Locate every Plasmodium parasite.
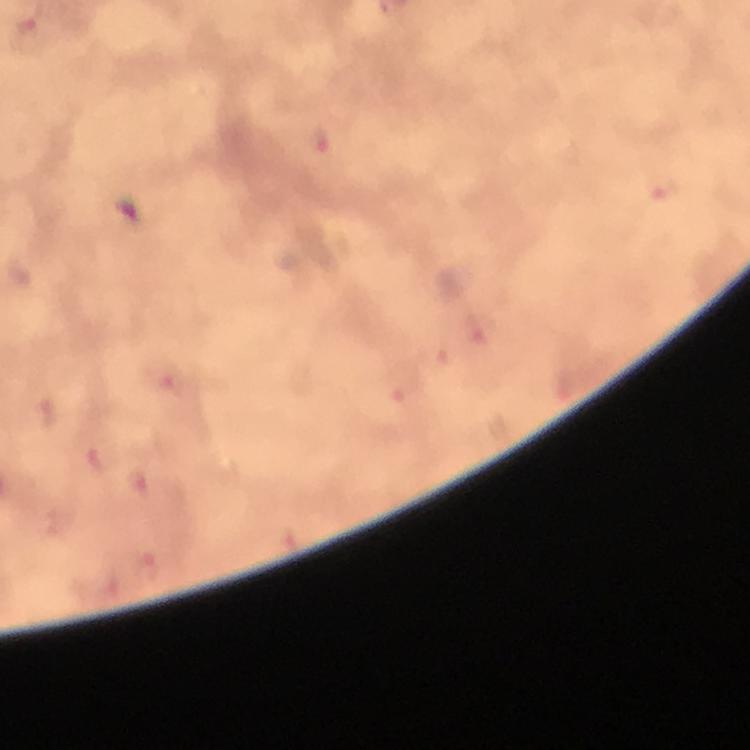

Approximate object centers, in pixels from the top-left corner.
Plasmodium parasites: (x=321, y=137), (x=661, y=187), (x=479, y=326), (x=171, y=380), (x=400, y=385), (x=48, y=412), (x=96, y=456), (x=138, y=483), (x=147, y=571).

Summary:
  - Immersion oil: applied
  - Capture: smartphone photograph through a microscope
  - Context: from a diagnostic examination for malaria
  - Stain: Giemsa
  - Preparation: thick blood film
  - Cropped from: a single field of view
  - Magnification: 100x
  - Image size: 750×750 pixels